Locate platelets.
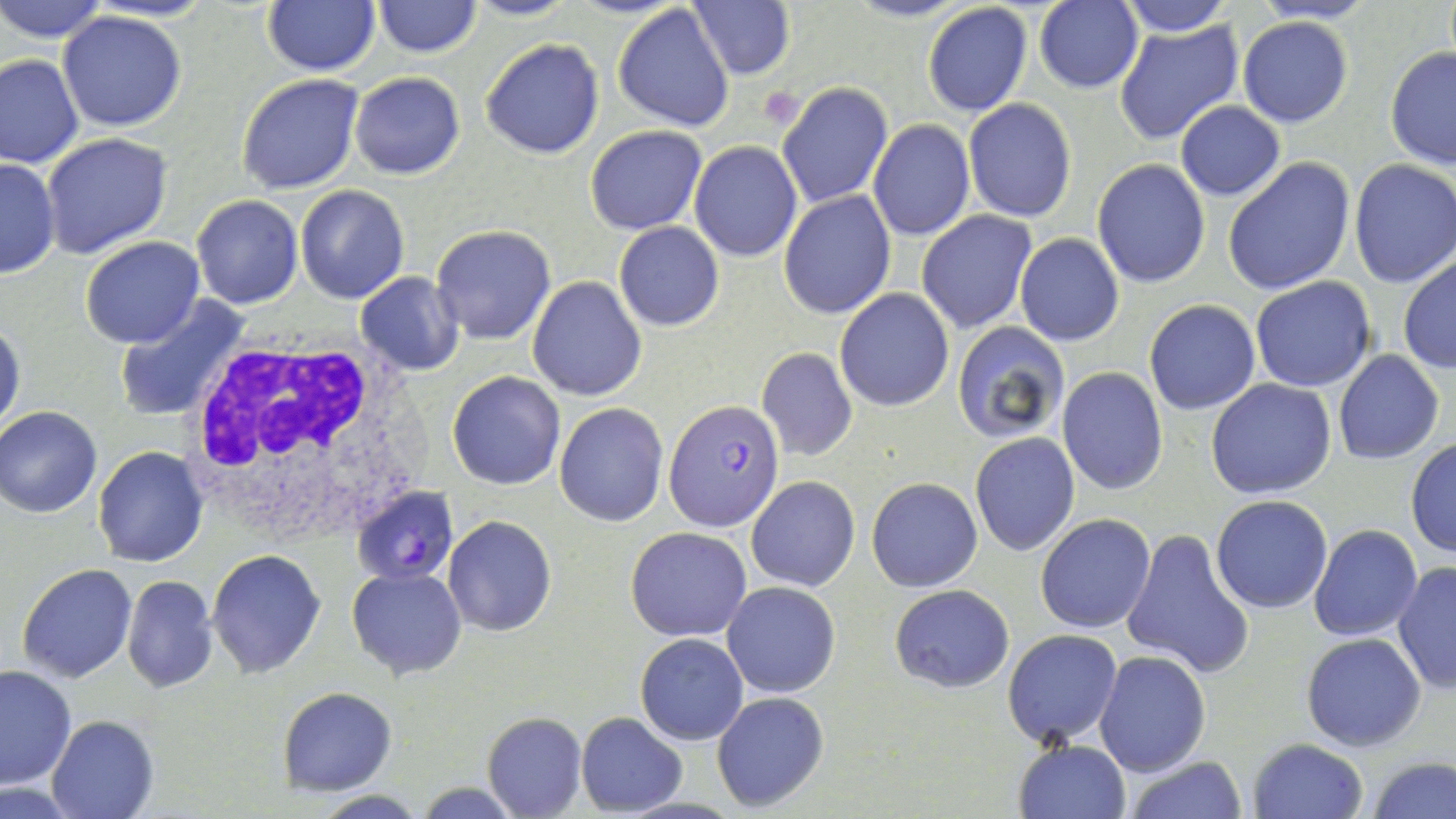

Approximate bounding boxes as (x1, y1, x2, y2) in pixels.
Platelets: (758, 87, 806, 129).

Uninfected red blood cell locations: (0, 0, 109, 43), (262, 0, 381, 76), (465, 0, 576, 22), (844, 0, 971, 24), (1115, 0, 1233, 36), (1253, 0, 1378, 23), (373, 1, 482, 58), (688, 1, 795, 80), (1033, 1, 1144, 93), (612, 3, 737, 132), (921, 3, 1033, 116), (59, 10, 186, 132), (1238, 17, 1353, 128), (1113, 19, 1244, 146), (480, 38, 604, 158), (1384, 46, 1456, 170), (0, 52, 83, 170), (349, 71, 466, 180), (235, 73, 363, 193), (775, 80, 892, 210), (963, 99, 1077, 222), (1175, 101, 1286, 200), (868, 119, 975, 241), (585, 125, 708, 235), (40, 132, 173, 261), (688, 141, 803, 262), (0, 156, 60, 278), (1222, 157, 1356, 296), (1092, 160, 1211, 289), (1348, 161, 1456, 288), (296, 184, 410, 303), (778, 190, 895, 320), (191, 195, 304, 309), (917, 211, 1036, 335), (614, 222, 724, 331), (431, 225, 558, 346), (1015, 234, 1124, 346), (79, 237, 204, 350), (1398, 254, 1456, 376), (356, 273, 464, 375), (1249, 275, 1376, 393), (528, 277, 647, 402), (833, 289, 956, 412), (114, 297, 249, 424), (1143, 299, 1260, 415), (0, 318, 25, 437), (950, 321, 1069, 445), (757, 347, 858, 462), (1334, 350, 1444, 464), (1057, 367, 1168, 495), (446, 371, 566, 490), (1205, 378, 1336, 499), (555, 402, 669, 527), (1, 407, 102, 518), (969, 431, 1080, 557), (1405, 439, 1456, 557), (91, 447, 209, 567), (747, 476, 860, 592), (866, 478, 983, 591), (1210, 493, 1334, 614), (1035, 513, 1157, 634), (442, 516, 557, 637), (1308, 524, 1422, 643), (625, 528, 751, 642), (1121, 528, 1254, 679), (206, 550, 326, 679), (1391, 560, 1456, 694), (16, 563, 137, 683), (347, 565, 467, 680), (121, 575, 218, 692), (720, 582, 841, 698), (889, 584, 1014, 694), (1003, 629, 1122, 746), (635, 633, 748, 744), (1301, 634, 1427, 752), (1095, 650, 1210, 775), (0, 664, 76, 788), (279, 687, 398, 794), (711, 691, 830, 812), (481, 713, 586, 819), (575, 713, 686, 815), (46, 714, 159, 818), (1247, 738, 1369, 819), (1012, 739, 1130, 819), (1123, 755, 1248, 819), (1366, 755, 1454, 818), (413, 781, 521, 818), (309, 791, 431, 819). Plasmodium falciparum-infected red blood cell locations: (664, 399, 785, 533), (353, 493, 456, 584). White blood cell locations: (178, 332, 423, 542). Slide-level diagnosis: Plasmodium falciparum. Optical microscopy. Image is 1456×819 pixels. Single field of view. Captured at 1000x magnification. May-Grünwald-Giemsa-stained preparation. Thin blood smear.